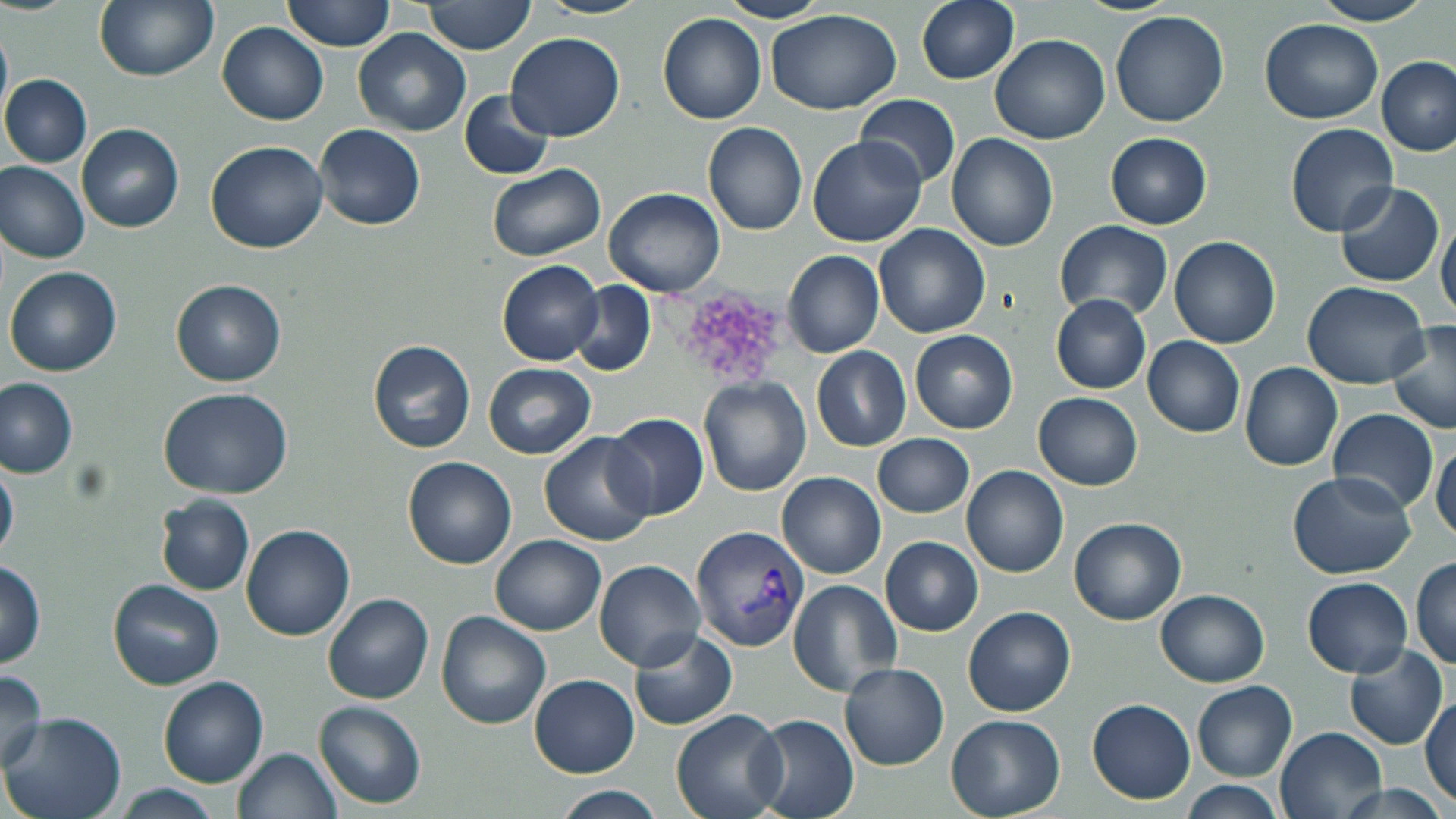

Approximate bounding boxes as (x1,y1)-(x2,y2) corner pairs in pixels. Platelet locations: (670,286)-(785,383). Uninfected red blood cell locations: (93,0)-(219,80), (284,0)-(397,52), (423,0)-(537,54), (535,0)-(651,19), (716,0)-(831,23), (917,0)-(1020,84), (1069,0)-(1180,15), (1310,0)-(1434,25), (765,8)-(904,114), (1109,10)-(1230,128), (658,13)-(768,123), (1260,18)-(1383,124), (218,22)-(329,124), (0,26)-(12,117), (353,27)-(472,138), (507,30)-(623,141), (991,34)-(1110,143), (1376,57)-(1454,156), (2,75)-(92,167), (461,90)-(554,180), (858,94)-(961,190), (703,122)-(808,236), (78,124)-(184,233), (315,124)-(426,231), (1285,124)-(1400,239), (947,132)-(1058,251), (1105,132)-(1212,230), (808,137)-(925,245), (204,140)-(329,253), (0,161)-(90,262), (488,163)-(605,261), (1335,181)-(1444,288), (605,187)-(727,296), (1436,219)-(1456,321), (1054,220)-(1172,319), (874,223)-(991,338), (1169,236)-(1280,348), (784,251)-(884,358), (497,260)-(604,366), (6,266)-(123,377), (170,279)-(286,385), (569,281)-(657,377), (1303,282)-(1430,387), (1051,296)-(1152,392), (1386,320)-(1456,437), (910,328)-(1019,434), (1143,336)-(1246,436), (368,339)-(477,453), (811,346)-(912,451), (1239,361)-(1342,470), (483,363)-(596,459), (0,377)-(79,478), (698,378)-(811,497), (158,387)-(294,498), (1034,392)-(1142,490), (1328,408)-(1439,513), (605,412)-(709,521), (873,433)-(975,518), (541,434)-(656,547), (1430,439)-(1456,542), (0,452)-(18,560), (403,456)-(518,569), (962,465)-(1068,576), (1288,470)-(1418,579), (778,472)-(885,577), (155,495)-(255,595), (1069,516)-(1186,624), (241,524)-(355,640), (490,535)-(605,636), (881,536)-(983,635), (1410,556)-(1456,669), (595,560)-(704,669), (0,561)-(47,667), (1303,576)-(1413,677), (109,579)-(224,690), (787,579)-(901,697), (1155,589)-(1268,686), (324,593)-(434,703), (962,606)-(1076,716), (438,610)-(553,729), (629,629)-(737,730), (1343,643)-(1447,750), (841,662)-(948,769), (0,672)-(48,773), (530,674)-(639,777), (160,677)-(269,787), (1192,680)-(1298,781), (1419,693)-(1456,805), (1087,698)-(1194,802), (315,701)-(427,809), (673,710)-(787,819), (3,712)-(127,819), (748,715)-(859,819), (946,715)-(1065,817), (1276,728)-(1388,819), (234,746)-(344,819), (1334,781)-(1450,819), (1180,782)-(1283,819), (110,784)-(224,819), (553,787)-(669,818). Plasmodium vivax-infected red blood cell locations: (689,524)-(808,652). Slide-level diagnosis: Plasmodium vivax. May-Grünwald-Giemsa-stained preparation. Image is 1456×819 pixels. One field of a larger specimen. Optical microscopy. Captured at 1000x magnification. Thin blood smear.